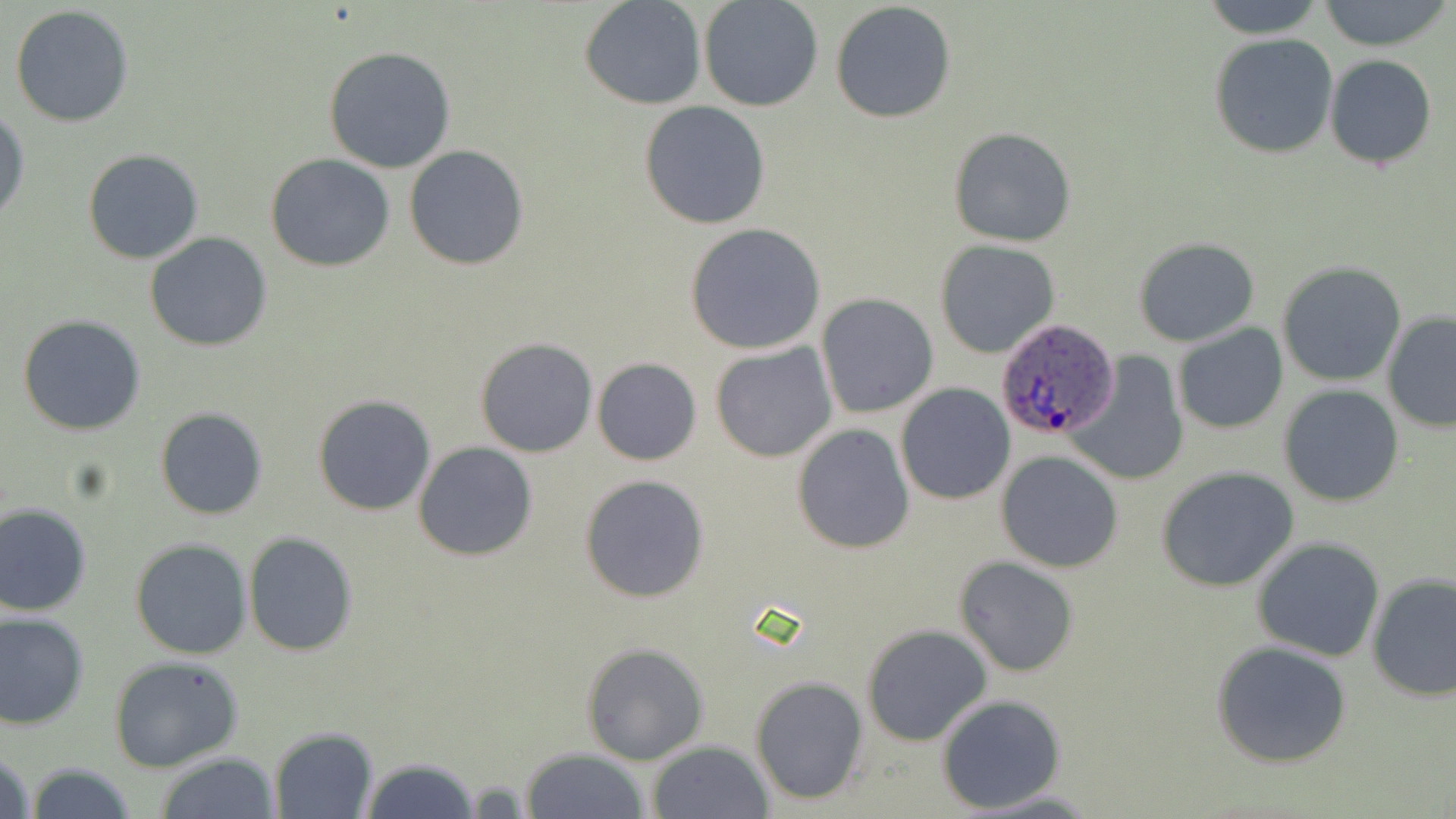

Summary:
  - Coordinate format: approximate bounding boxes as named x1/y1/x2/y2 corners in pixels
  - Uninfected red blood cell locations: (x1=1199, y1=0, x2=1327, y2=37), (x1=1318, y1=0, x2=1450, y2=51), (x1=579, y1=1, x2=707, y2=110), (x1=698, y1=1, x2=823, y2=113), (x1=830, y1=1, x2=957, y2=125), (x1=8, y1=5, x2=135, y2=128), (x1=1209, y1=34, x2=1338, y2=159), (x1=322, y1=46, x2=457, y2=174), (x1=1324, y1=55, x2=1437, y2=170), (x1=640, y1=101, x2=770, y2=229), (x1=1, y1=109, x2=29, y2=225), (x1=948, y1=126, x2=1076, y2=247), (x1=404, y1=145, x2=530, y2=269), (x1=81, y1=149, x2=204, y2=264), (x1=265, y1=154, x2=395, y2=272), (x1=685, y1=223, x2=826, y2=355), (x1=144, y1=231, x2=273, y2=352), (x1=1133, y1=238, x2=1259, y2=348), (x1=935, y1=241, x2=1058, y2=358), (x1=1275, y1=262, x2=1406, y2=387), (x1=817, y1=293, x2=939, y2=418), (x1=1381, y1=310, x2=1456, y2=434), (x1=17, y1=314, x2=148, y2=436), (x1=1172, y1=324, x2=1288, y2=433), (x1=475, y1=336, x2=600, y2=457), (x1=710, y1=343, x2=837, y2=462), (x1=1066, y1=351, x2=1189, y2=487), (x1=592, y1=357, x2=703, y2=466), (x1=1278, y1=382, x2=1404, y2=507), (x1=896, y1=384, x2=1016, y2=504), (x1=313, y1=393, x2=436, y2=516), (x1=154, y1=407, x2=269, y2=520), (x1=791, y1=423, x2=914, y2=553), (x1=413, y1=441, x2=538, y2=562), (x1=996, y1=450, x2=1124, y2=573), (x1=1156, y1=466, x2=1298, y2=592), (x1=579, y1=475, x2=710, y2=604), (x1=0, y1=503, x2=93, y2=616), (x1=242, y1=531, x2=359, y2=657), (x1=1252, y1=536, x2=1386, y2=663), (x1=130, y1=537, x2=252, y2=659), (x1=954, y1=557, x2=1078, y2=678), (x1=1366, y1=574, x2=1455, y2=702), (x1=0, y1=611, x2=90, y2=730), (x1=862, y1=625, x2=992, y2=747), (x1=1210, y1=640, x2=1356, y2=770), (x1=580, y1=642, x2=710, y2=766), (x1=108, y1=655, x2=245, y2=773), (x1=750, y1=676, x2=869, y2=805), (x1=936, y1=695, x2=1064, y2=813), (x1=269, y1=727, x2=378, y2=818), (x1=646, y1=741, x2=774, y2=819), (x1=1, y1=745, x2=36, y2=819), (x1=521, y1=748, x2=649, y2=819), (x1=153, y1=752, x2=282, y2=818), (x1=357, y1=756, x2=483, y2=819), (x1=22, y1=762, x2=140, y2=819), (x1=962, y1=786, x2=1105, y2=816)
  - Plasmodium ovale-infected red blood cell locations: (x1=994, y1=320, x2=1121, y2=442)
  - Slide-level diagnosis: Plasmodium ovale
  - Magnification: 1000x
  - Image size: 1456×819 pixels
  - Field of view: one of a larger specimen
  - Stain: May-Grünwald-Giemsa
  - Modality: optical microscopy
  - Preparation: thin blood film